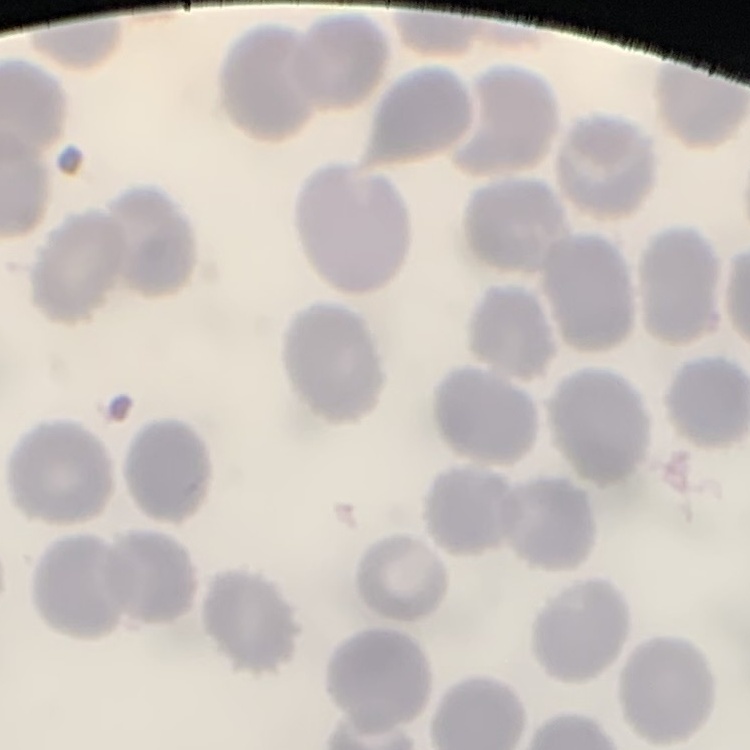
Summary:
  - Erythrocyte morphology: no rouleaux formation
  - Stain: Field's or Giemsa
  - Image type: square crop of a larger photomicrograph
  - Preparation: thin peripheral smear